State which parasite is depicted.
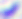
Toxoplasma gondii.

Micrograph. 400x magnification.